Classify this cell by malaria status.
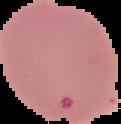
It is parasitized.

Segmented cell region on a black background. Image is 121×124 pixels. From a thin blood smear.